Name the blood parasite species.
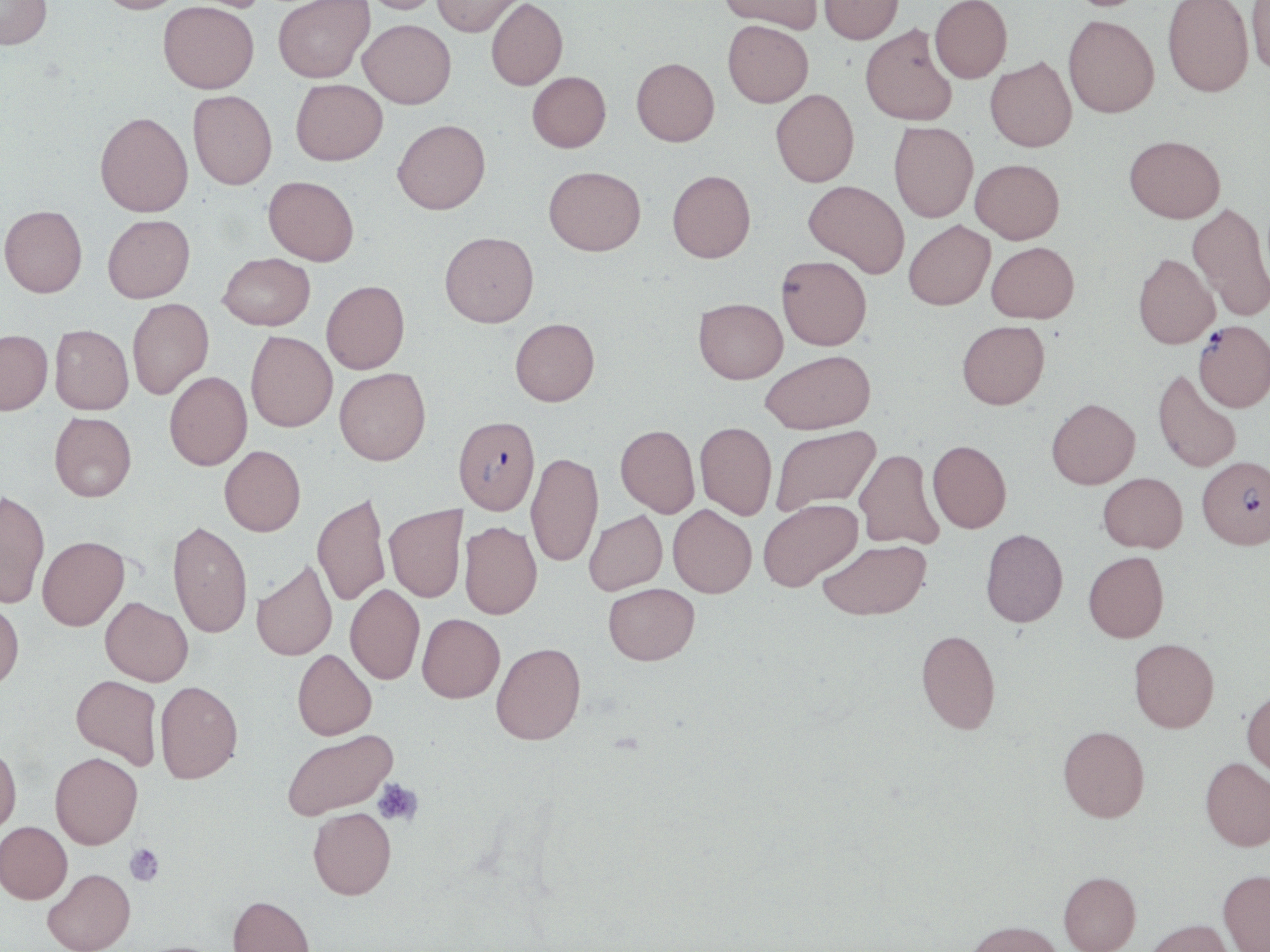
Plasmodium falciparum.

Approximate bounding boxes as named x1/y1/x2/y2 corners in pixels. Plasmodium falciparum-infected red blood cell locations: (x1=1193, y1=320, x2=1270, y2=412), (x1=453, y1=415, x2=540, y2=514), (x1=1197, y1=456, x2=1270, y2=549). Platelet locations: (x1=373, y1=778, x2=423, y2=825), (x1=125, y1=843, x2=164, y2=887). Uninfected red blood cell locations: (x1=0, y1=0, x2=52, y2=50), (x1=95, y1=0, x2=187, y2=14), (x1=360, y1=0, x2=444, y2=14), (x1=432, y1=0, x2=524, y2=36), (x1=486, y1=0, x2=568, y2=90), (x1=719, y1=0, x2=823, y2=34), (x1=819, y1=0, x2=903, y2=44), (x1=930, y1=0, x2=1012, y2=82), (x1=1163, y1=0, x2=1254, y2=97), (x1=1246, y1=0, x2=1270, y2=76), (x1=158, y1=1, x2=259, y2=93), (x1=272, y1=1, x2=374, y2=83), (x1=1063, y1=14, x2=1160, y2=118), (x1=358, y1=19, x2=456, y2=109), (x1=723, y1=20, x2=813, y2=107), (x1=860, y1=24, x2=958, y2=125), (x1=985, y1=56, x2=1077, y2=152), (x1=631, y1=57, x2=719, y2=146), (x1=527, y1=72, x2=611, y2=152), (x1=291, y1=79, x2=387, y2=165), (x1=771, y1=89, x2=859, y2=186), (x1=187, y1=90, x2=277, y2=189), (x1=95, y1=111, x2=193, y2=217), (x1=392, y1=119, x2=490, y2=214), (x1=889, y1=122, x2=978, y2=222), (x1=1124, y1=134, x2=1226, y2=223), (x1=970, y1=159, x2=1064, y2=243), (x1=544, y1=166, x2=646, y2=255), (x1=667, y1=170, x2=756, y2=262), (x1=263, y1=176, x2=359, y2=265), (x1=804, y1=180, x2=910, y2=278), (x1=1187, y1=203, x2=1270, y2=320), (x1=0, y1=205, x2=87, y2=297), (x1=102, y1=214, x2=195, y2=303), (x1=904, y1=220, x2=995, y2=310), (x1=440, y1=231, x2=539, y2=327), (x1=987, y1=242, x2=1079, y2=323), (x1=218, y1=253, x2=315, y2=330), (x1=1133, y1=253, x2=1219, y2=348), (x1=776, y1=255, x2=871, y2=350), (x1=321, y1=280, x2=409, y2=373), (x1=693, y1=297, x2=787, y2=383), (x1=127, y1=298, x2=213, y2=399), (x1=510, y1=318, x2=600, y2=406), (x1=957, y1=320, x2=1050, y2=409), (x1=50, y1=325, x2=134, y2=414), (x1=0, y1=329, x2=53, y2=414), (x1=246, y1=331, x2=337, y2=432), (x1=761, y1=349, x2=875, y2=434), (x1=335, y1=367, x2=431, y2=465), (x1=1152, y1=368, x2=1242, y2=473), (x1=164, y1=371, x2=252, y2=470), (x1=1046, y1=398, x2=1140, y2=489), (x1=49, y1=412, x2=137, y2=502), (x1=695, y1=421, x2=777, y2=520), (x1=615, y1=425, x2=700, y2=517), (x1=771, y1=426, x2=880, y2=515), (x1=927, y1=440, x2=1011, y2=532), (x1=219, y1=445, x2=306, y2=536), (x1=854, y1=448, x2=943, y2=549), (x1=526, y1=452, x2=603, y2=566), (x1=1098, y1=472, x2=1187, y2=552), (x1=0, y1=489, x2=50, y2=608), (x1=312, y1=492, x2=390, y2=606), (x1=758, y1=498, x2=863, y2=591), (x1=385, y1=504, x2=466, y2=602), (x1=668, y1=504, x2=757, y2=597), (x1=584, y1=510, x2=667, y2=595), (x1=168, y1=520, x2=253, y2=638), (x1=459, y1=521, x2=542, y2=619), (x1=980, y1=528, x2=1068, y2=627), (x1=37, y1=536, x2=129, y2=630), (x1=818, y1=539, x2=931, y2=620), (x1=1083, y1=551, x2=1169, y2=642), (x1=251, y1=559, x2=337, y2=660), (x1=603, y1=582, x2=700, y2=665), (x1=345, y1=584, x2=425, y2=684), (x1=100, y1=596, x2=193, y2=685), (x1=0, y1=597, x2=24, y2=691), (x1=417, y1=613, x2=505, y2=702), (x1=916, y1=629, x2=1001, y2=734), (x1=1129, y1=638, x2=1219, y2=732), (x1=491, y1=642, x2=586, y2=744), (x1=292, y1=649, x2=377, y2=740), (x1=71, y1=675, x2=163, y2=770), (x1=155, y1=680, x2=243, y2=783), (x1=1242, y1=687, x2=1270, y2=778), (x1=1058, y1=725, x2=1150, y2=822), (x1=282, y1=729, x2=397, y2=819), (x1=0, y1=744, x2=22, y2=836), (x1=50, y1=752, x2=142, y2=849), (x1=1201, y1=756, x2=1270, y2=851), (x1=308, y1=806, x2=396, y2=899), (x1=0, y1=821, x2=72, y2=903), (x1=43, y1=868, x2=135, y2=952), (x1=1218, y1=869, x2=1270, y2=952), (x1=1059, y1=871, x2=1141, y2=952), (x1=228, y1=895, x2=315, y2=952), (x1=1144, y1=918, x2=1236, y2=952), (x1=965, y1=920, x2=1064, y2=952). Thin blood film. May-Grünwald-Giemsa-stained preparation. 1000x magnification. Image is 1270×952 pixels. Single field of view. Optical microscopy.